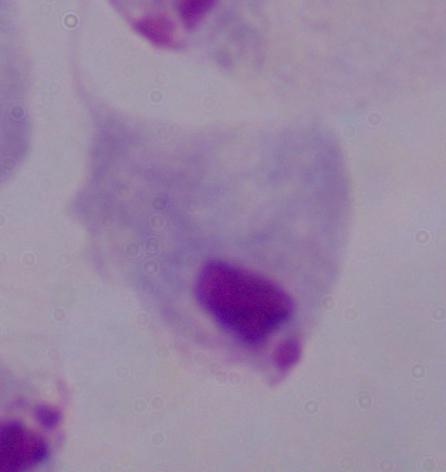

identification = trichomonad
modality = photomicrograph
magnification = 1000x